Identify the parasite.
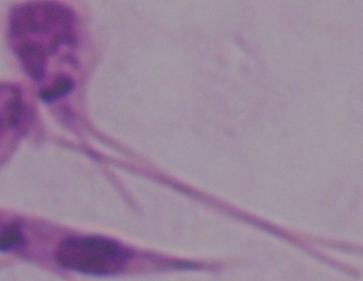
This is Leishmania.

Micrograph. Captured at 1000x magnification.